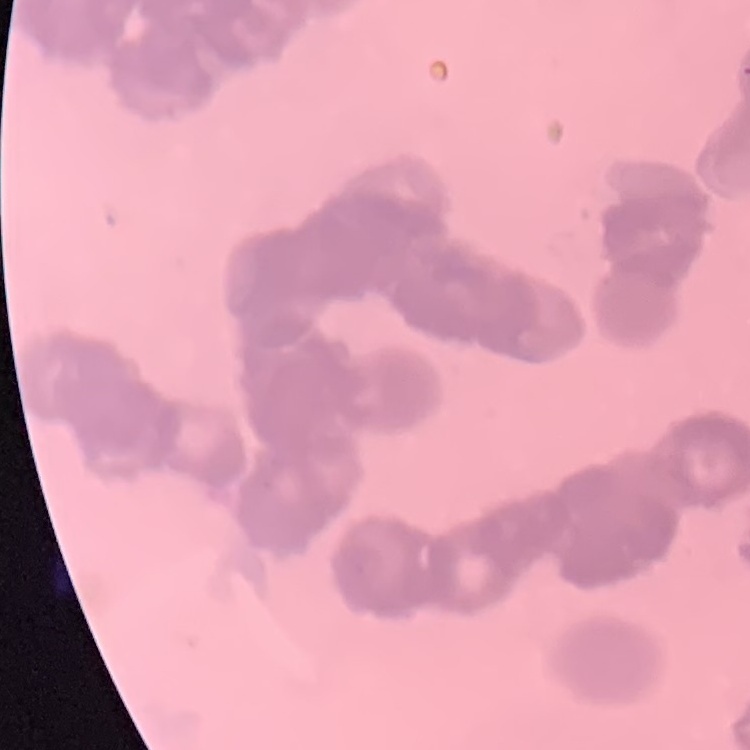

Summary:
  - Erythrocyte morphology: rouleaux formation
  - Stain: Field's or Giemsa
  - Preparation: thin blood film
  - Image type: square crop of a larger photomicrograph